Describe the morphology of the erythrocytes.
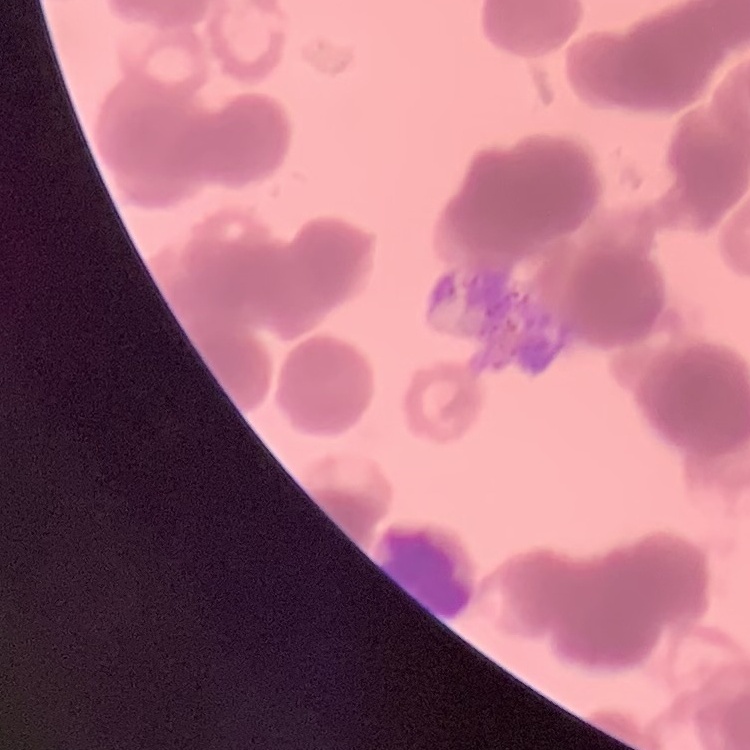

Rouleaux formation.

Summary:
  - Preparation: thin blood smear
  - Stain: Field's or Giemsa
  - Image type: square crop of a larger photomicrograph